Name the parasite shown.
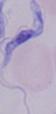
A trypanosome.

modality: photomicrograph
magnification: 1000x